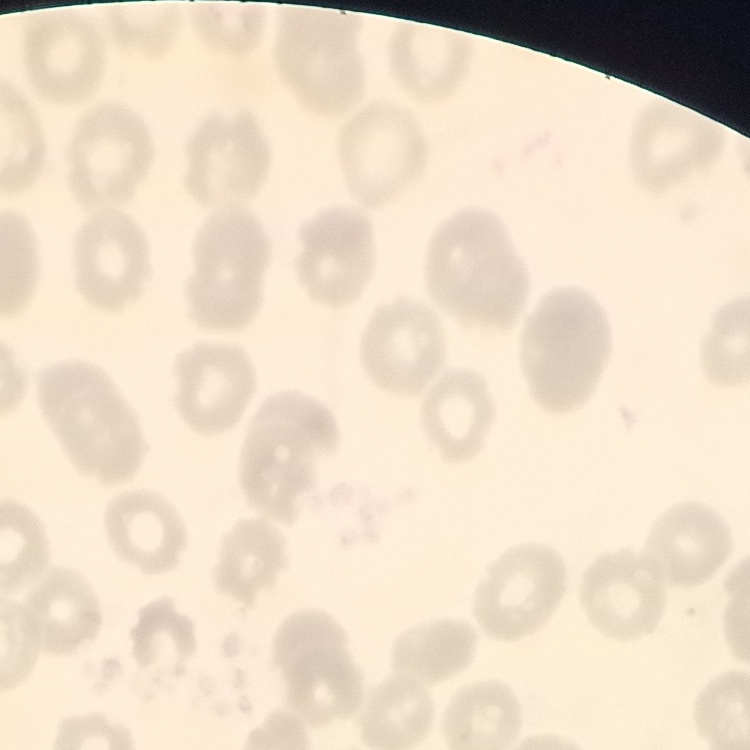
The erythrocytes exhibit no rouleaux formation. Stained with either Field's or Giemsa. Thin blood smear. Square crop of a larger photomicrograph.